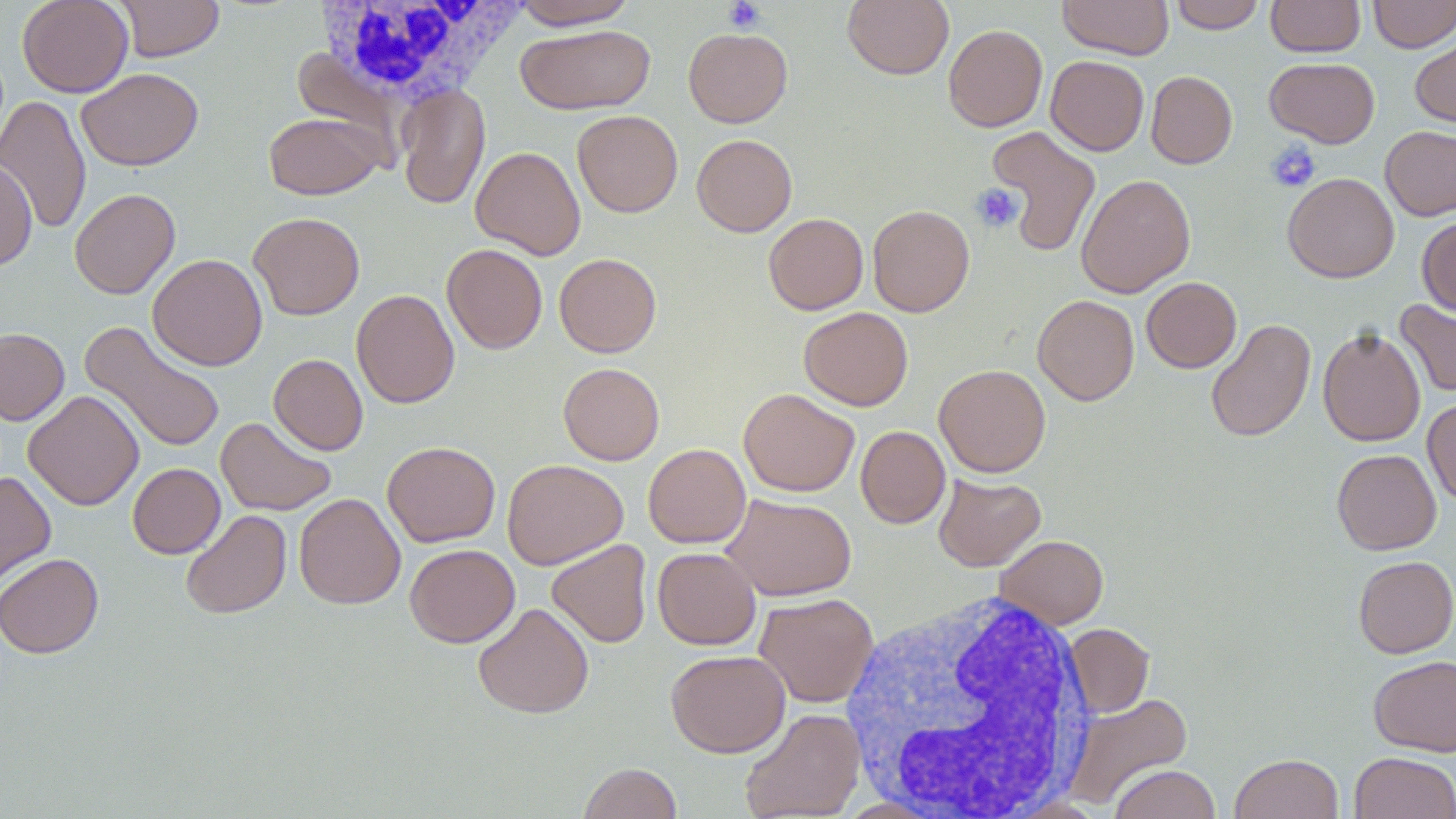
Approximate bounding boxes as (x1, y1, x2, y2) in pixels. Uninfected red blood cell locations: (17, 0, 134, 97), (114, 0, 224, 62), (507, 0, 641, 30), (843, 0, 954, 80), (1057, 0, 1174, 59), (1167, 0, 1266, 33), (1266, 0, 1365, 57), (1368, 0, 1456, 53), (342, 1, 500, 109), (515, 24, 655, 115), (943, 24, 1048, 132), (683, 27, 793, 127), (1410, 31, 1456, 133), (1046, 55, 1149, 156), (1265, 57, 1380, 148), (76, 68, 203, 171), (1146, 71, 1237, 168), (396, 83, 491, 210), (0, 95, 91, 235), (572, 110, 683, 217), (263, 111, 384, 200), (1380, 125, 1456, 221), (986, 127, 1101, 256), (692, 134, 797, 237), (471, 146, 585, 260), (0, 158, 37, 271), (1282, 172, 1399, 283), (1075, 174, 1196, 298), (70, 188, 180, 299), (868, 205, 975, 317), (248, 212, 365, 320), (763, 212, 868, 315), (1417, 215, 1456, 315), (442, 243, 547, 353), (554, 252, 661, 357), (148, 253, 268, 371), (1141, 277, 1242, 373), (351, 289, 460, 408), (1032, 295, 1139, 406), (1395, 300, 1456, 397), (798, 307, 913, 410), (1205, 318, 1316, 443), (80, 321, 226, 454), (1317, 326, 1426, 447), (0, 328, 69, 425), (269, 353, 368, 455), (558, 362, 665, 465), (934, 363, 1051, 477), (738, 388, 859, 497), (23, 389, 144, 511), (1422, 398, 1456, 505), (216, 416, 337, 516), (856, 425, 950, 528), (382, 440, 501, 547), (643, 443, 751, 548), (1332, 449, 1441, 555), (502, 459, 628, 570), (127, 463, 225, 558), (0, 471, 56, 589), (933, 473, 1046, 571), (294, 493, 406, 610), (720, 493, 857, 601), (180, 509, 292, 619), (994, 535, 1109, 629), (546, 539, 652, 648), (405, 544, 520, 647), (652, 547, 761, 649), (0, 553, 104, 658), (1353, 555, 1456, 658), (754, 592, 879, 708), (472, 602, 594, 719), (1064, 623, 1154, 717), (665, 649, 790, 757), (1368, 655, 1456, 756), (1064, 692, 1193, 809), (739, 707, 865, 818), (1349, 751, 1456, 819), (1230, 753, 1344, 819), (577, 762, 682, 819), (1109, 764, 1221, 818). Platelet locations: (723, 0, 765, 33), (1264, 140, 1321, 192), (970, 183, 1025, 233). White blood cell locations: (312, 1, 527, 105), (839, 586, 1098, 818). Slide-level diagnosis: no evidence of blood parasites. Optical microscopy. Thin blood smear. Captured at 1000x magnification. Image is 1456×819 pixels. Single field of view. May-Grünwald-Giemsa-stained preparation.